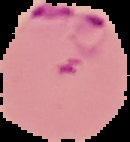

From a thin blood film. Cell region segmented out of the field of view; the surrounding area is masked to black. Result: malaria parasites detected. Image is 130×142 pixels.